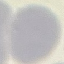
malaria status = uninfected
capture = smartphone camera at the microscope eyepiece
stain = Giemsa
image type = automatically extracted cell patch, resized to 64 × 64 pixels
preparation = thin blood smear